Locate every uninfected red blood cell.
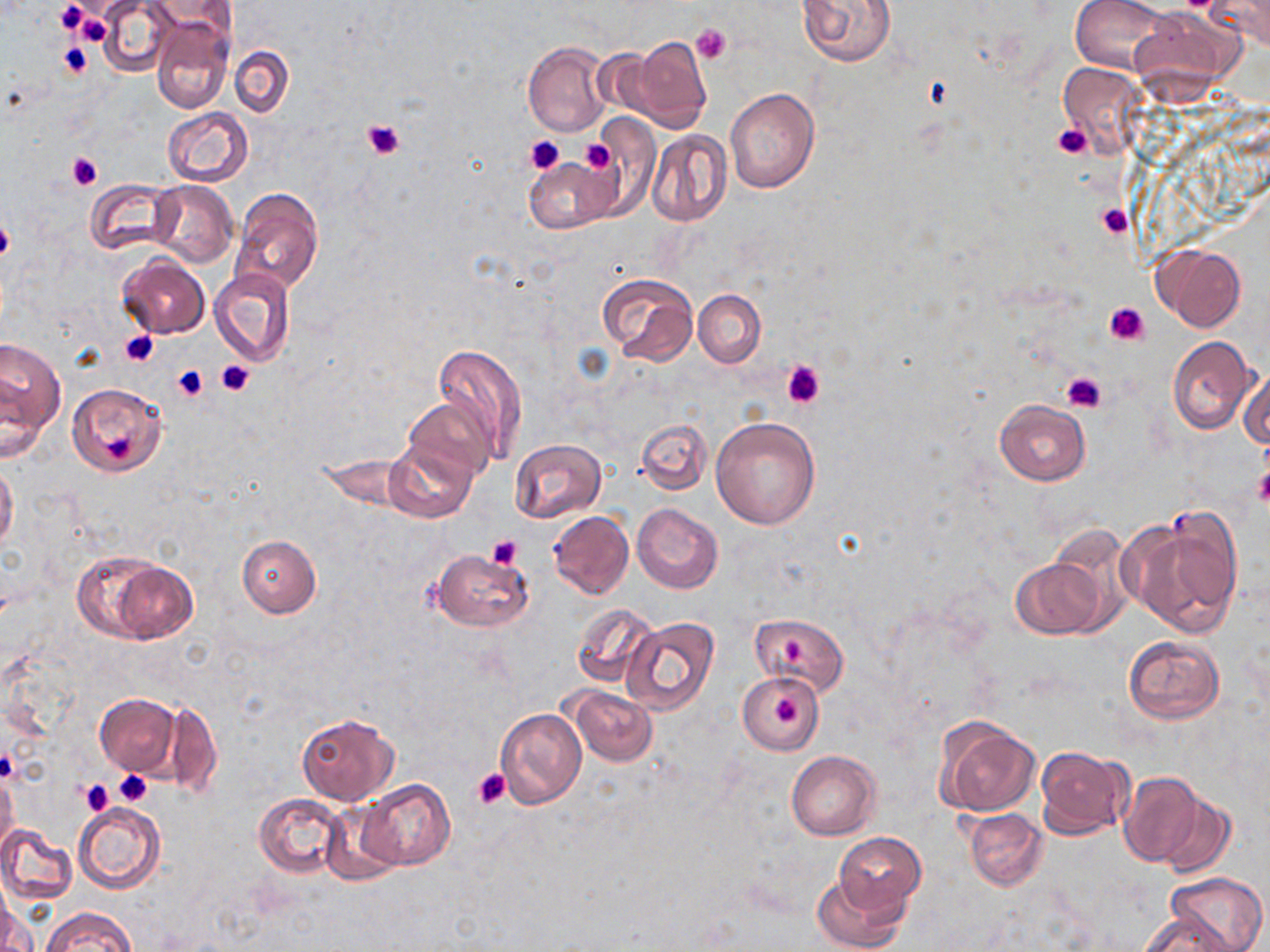
Approximate bounding boxes as named x1/y1/x2/y2 corners in pixels.
Uninfected red blood cells: (x1=97, y1=0, x2=177, y2=77), (x1=148, y1=0, x2=236, y2=42), (x1=797, y1=0, x2=897, y2=66), (x1=1071, y1=0, x2=1170, y2=74), (x1=1205, y1=0, x2=1270, y2=49), (x1=1131, y1=8, x2=1243, y2=94), (x1=151, y1=17, x2=233, y2=113), (x1=623, y1=37, x2=712, y2=133), (x1=523, y1=42, x2=611, y2=138), (x1=228, y1=44, x2=294, y2=119), (x1=1058, y1=61, x2=1149, y2=159), (x1=724, y1=88, x2=819, y2=192), (x1=161, y1=108, x2=254, y2=187), (x1=587, y1=117, x2=660, y2=211), (x1=645, y1=130, x2=733, y2=227), (x1=526, y1=160, x2=614, y2=234), (x1=86, y1=178, x2=182, y2=257), (x1=148, y1=181, x2=237, y2=269), (x1=231, y1=188, x2=325, y2=295), (x1=1153, y1=244, x2=1246, y2=332), (x1=117, y1=254, x2=209, y2=339), (x1=211, y1=267, x2=295, y2=365), (x1=597, y1=271, x2=699, y2=366), (x1=693, y1=289, x2=767, y2=368), (x1=1, y1=335, x2=66, y2=454), (x1=1166, y1=337, x2=1260, y2=435), (x1=433, y1=344, x2=530, y2=466), (x1=1236, y1=369, x2=1269, y2=449), (x1=66, y1=383, x2=168, y2=478), (x1=404, y1=395, x2=495, y2=481), (x1=994, y1=399, x2=1091, y2=485), (x1=711, y1=415, x2=821, y2=528), (x1=637, y1=419, x2=711, y2=495), (x1=384, y1=438, x2=479, y2=525), (x1=510, y1=439, x2=607, y2=523), (x1=0, y1=462, x2=19, y2=556), (x1=632, y1=502, x2=723, y2=593), (x1=1123, y1=510, x2=1244, y2=638), (x1=549, y1=511, x2=633, y2=599), (x1=237, y1=535, x2=321, y2=618), (x1=430, y1=548, x2=534, y2=632), (x1=73, y1=551, x2=195, y2=643), (x1=1011, y1=555, x2=1109, y2=639), (x1=571, y1=603, x2=660, y2=690), (x1=750, y1=614, x2=849, y2=696), (x1=622, y1=617, x2=722, y2=716), (x1=1123, y1=635, x2=1224, y2=723), (x1=738, y1=672, x2=823, y2=752), (x1=567, y1=687, x2=658, y2=766), (x1=93, y1=693, x2=181, y2=776), (x1=157, y1=698, x2=220, y2=798), (x1=495, y1=708, x2=587, y2=808), (x1=294, y1=714, x2=398, y2=804), (x1=934, y1=717, x2=1039, y2=816), (x1=1034, y1=747, x2=1133, y2=839), (x1=787, y1=750, x2=881, y2=840), (x1=0, y1=771, x2=19, y2=854), (x1=1118, y1=772, x2=1208, y2=868), (x1=358, y1=780, x2=455, y2=870), (x1=255, y1=793, x2=348, y2=879), (x1=1154, y1=793, x2=1236, y2=879), (x1=72, y1=802, x2=166, y2=894), (x1=320, y1=802, x2=406, y2=885), (x1=964, y1=808, x2=1049, y2=891), (x1=0, y1=825, x2=77, y2=904), (x1=835, y1=833, x2=926, y2=918), (x1=1164, y1=871, x2=1267, y2=951), (x1=813, y1=872, x2=907, y2=952), (x1=2, y1=907, x2=37, y2=952), (x1=43, y1=907, x2=136, y2=952), (x1=1140, y1=911, x2=1235, y2=951).

Summary:
  - Platelet locations: (x1=55, y1=1, x2=87, y2=34), (x1=73, y1=9, x2=112, y2=47), (x1=690, y1=23, x2=731, y2=65), (x1=57, y1=42, x2=94, y2=78), (x1=362, y1=117, x2=408, y2=160), (x1=1053, y1=122, x2=1091, y2=158), (x1=526, y1=135, x2=564, y2=175), (x1=580, y1=139, x2=617, y2=175), (x1=66, y1=152, x2=101, y2=191), (x1=1097, y1=203, x2=1133, y2=239), (x1=0, y1=214, x2=14, y2=264), (x1=1104, y1=301, x2=1151, y2=347), (x1=119, y1=330, x2=159, y2=368), (x1=216, y1=359, x2=255, y2=397), (x1=780, y1=359, x2=826, y2=409), (x1=172, y1=364, x2=209, y2=403), (x1=1060, y1=369, x2=1108, y2=412), (x1=104, y1=436, x2=136, y2=463), (x1=1254, y1=466, x2=1270, y2=508), (x1=487, y1=534, x2=523, y2=568), (x1=781, y1=637, x2=808, y2=662), (x1=775, y1=697, x2=805, y2=728), (x1=0, y1=748, x2=19, y2=782), (x1=473, y1=769, x2=512, y2=810), (x1=115, y1=771, x2=152, y2=806), (x1=81, y1=778, x2=115, y2=816)
  - Slide-level diagnosis: no evidence of blood parasites
  - Magnification: 1000x
  - Field of view: single
  - Image size: 1270×952 pixels
  - Modality: light microscopy
  - Stain: May-Grünwald-Giemsa
  - Preparation: thin blood film